Locate and identify every blood parasite.
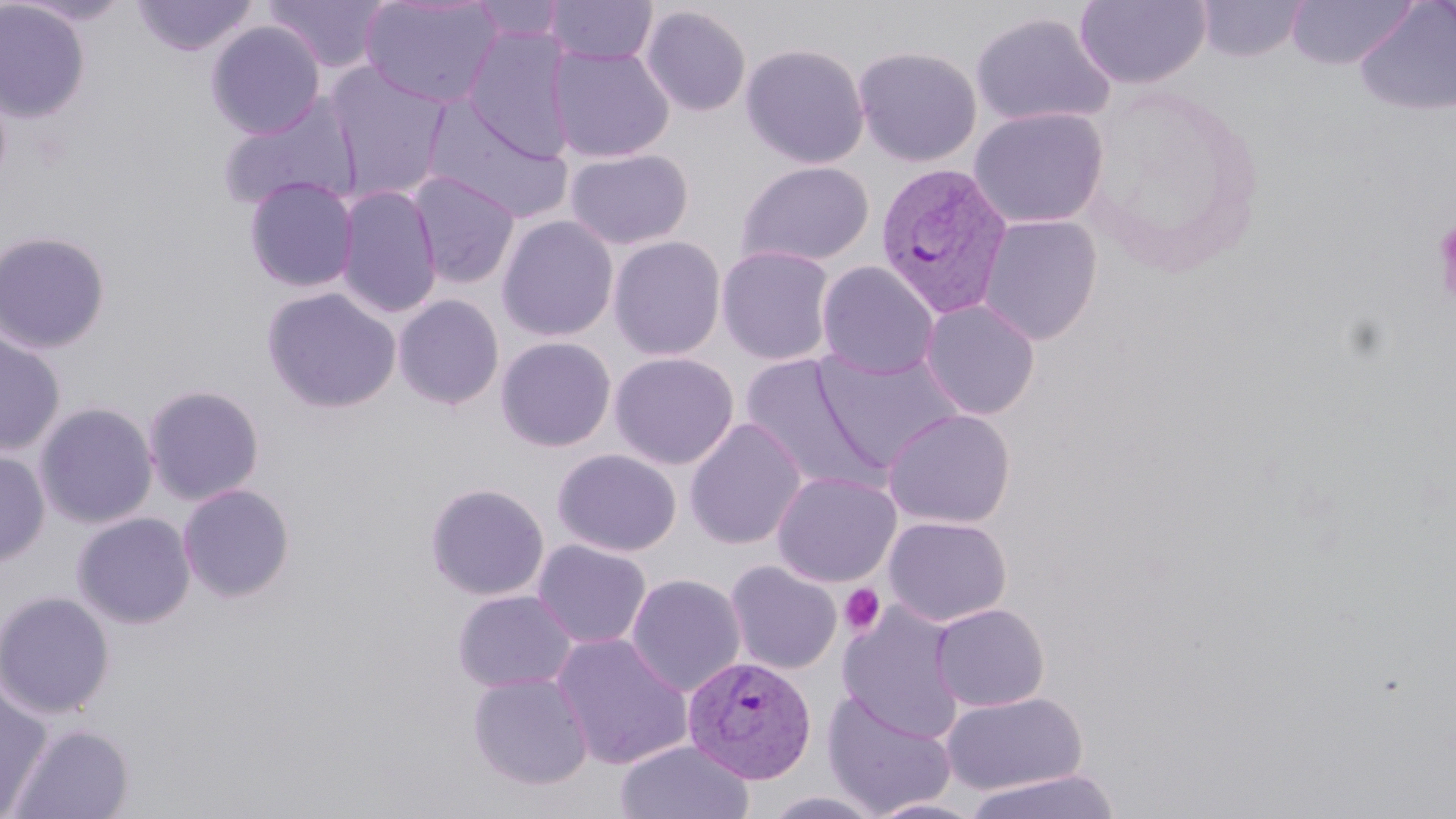

Approximate bounding boxes as (x1,y1)-(x2,y2) corner pairs in pixels.
Plasmodium vivax-infected red blood cells: (874,161)-(1013,318), (682,655)-(816,784).
No Plasmodium falciparum, Plasmodium ovale, Plasmodium malariae, Babesia divergens, or Trypanosoma brucei observed.

slide-level diagnosis = Plasmodium vivax
stain = May-Grünwald-Giemsa
modality = light microscopy
field of view = one of a larger specimen
preparation = thin blood film
uninfected red blood cell locations = approximate bounding boxes as (x1,y1)-(x2,y2) corner pairs in pixels: (13,0)-(136,26), (131,0)-(260,57), (261,0)-(394,74), (359,0)-(503,108), (544,0)-(658,65), (1075,0)-(1211,89), (1195,0)-(1309,62), (1285,0)-(1418,70), (0,1)-(92,124), (464,1)-(571,44), (1353,2)-(1456,117), (640,5)-(752,116), (969,10)-(1117,129), (205,21)-(326,139), (462,26)-(577,160), (547,43)-(674,163), (740,43)-(870,169), (852,45)-(982,167), (324,62)-(452,200), (215,92)-(362,212), (422,99)-(570,222), (969,107)-(1109,229), (564,148)-(693,250), (736,160)-(874,267), (407,171)-(520,288), (243,176)-(359,292), (335,184)-(442,319), (497,214)-(619,342), (977,215)-(1102,345), (0,230)-(112,354), (608,236)-(726,361), (716,245)-(835,366), (816,261)-(939,379), (261,286)-(402,414), (392,294)-(505,410), (919,298)-(1040,419), (0,328)-(66,456), (495,336)-(617,452), (812,349)-(963,472), (609,351)-(739,470), (740,356)-(882,491), (142,384)-(265,506), (34,401)-(158,529), (882,409)-(1015,528), (684,417)-(807,550), (0,447)-(51,569), (552,448)-(682,557), (772,471)-(901,588), (177,482)-(296,603), (425,482)-(550,601), (72,512)-(196,629), (884,515)-(1011,626), (532,539)-(652,649), (724,560)-(843,674), (626,573)-(746,697), (451,589)-(578,694), (0,590)-(116,719), (838,603)-(965,741), (930,603)-(1049,711), (552,633)-(693,770), (467,672)-(594,790), (0,680)-(55,817), (821,690)-(957,817), (941,691)-(1087,794), (8,723)-(136,819), (615,740)-(754,819), (961,769)-(1121,819), (761,790)-(888,818), (866,798)-(987,819)
image size = 1456×819 pixels
platelet locations = approximate bounding boxes as (x1,y1)-(x2,y2) corner pairs in pixels: (1433,218)-(1456,307), (839,583)-(886,637)
magnification = 1000x